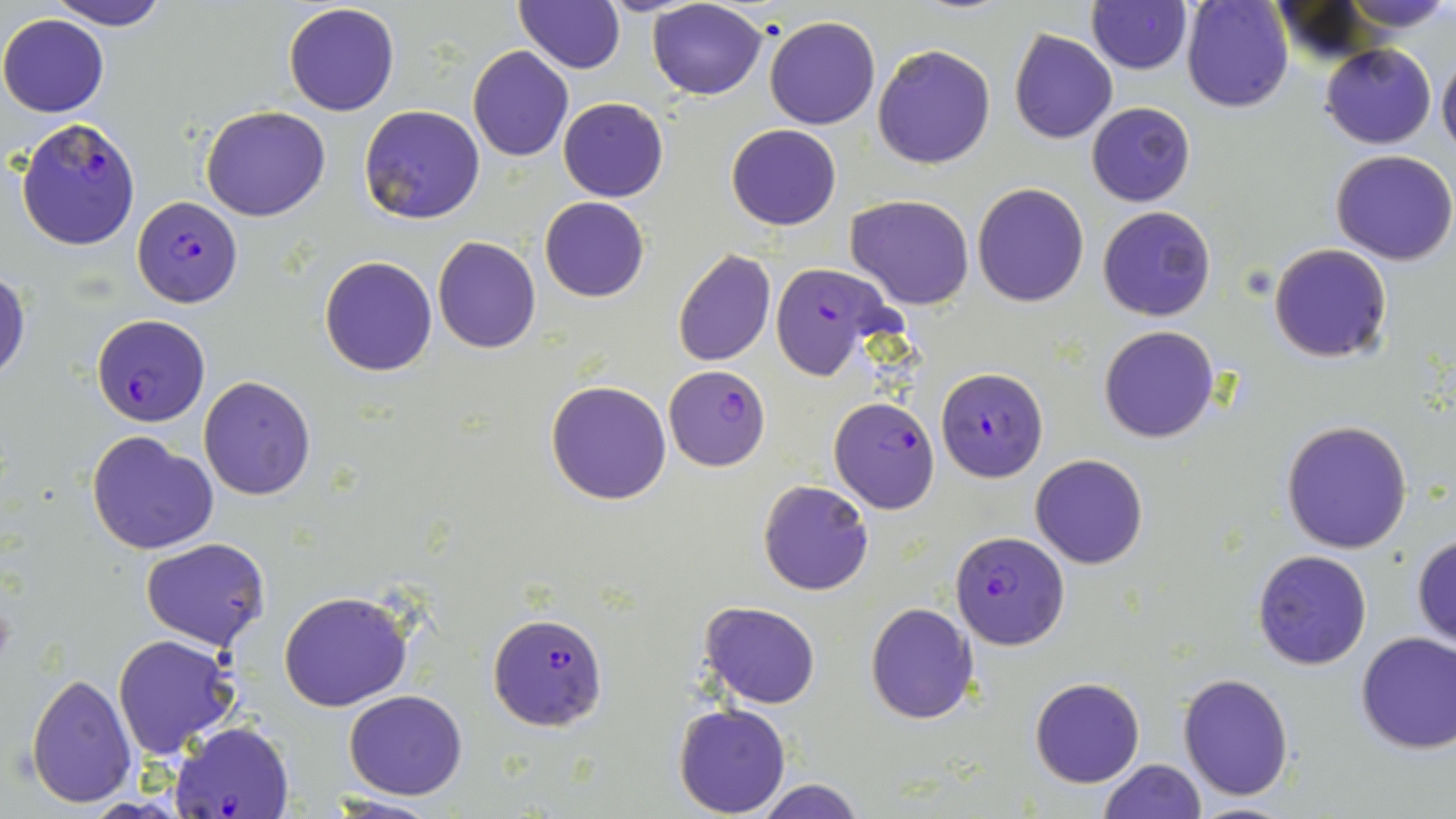

slide_level_diagnosis: Plasmodium falciparum
image_size: 1456×819 pixels
field_of_view: one of a larger specimen
modality: optical microscopy
uninfected_red_blood_cell_locations: 'approximate bounding boxes as named x1/y1/x2/y2 corners in pixels: (x1=48, y1=0, x2=170, y2=30), (x1=1182, y1=0, x2=1293, y2=113), (x1=1341, y1=0, x2=1452, y2=35), (x1=513, y1=1, x2=625, y2=73), (x1=1087, y1=1, x2=1192, y2=75), (x1=647, y1=2, x2=768, y2=99), (x1=282, y1=3, x2=400, y2=116), (x1=0, y1=12, x2=109, y2=117), (x1=763, y1=16, x2=881, y2=130), (x1=1009, y1=30, x2=1118, y2=145), (x1=872, y1=43, x2=996, y2=169), (x1=1320, y1=43, x2=1437, y2=148), (x1=467, y1=47, x2=575, y2=162), (x1=1437, y1=50, x2=1456, y2=159), (x1=558, y1=98, x2=669, y2=202), (x1=1086, y1=102, x2=1195, y2=206), (x1=359, y1=104, x2=486, y2=225), (x1=201, y1=105, x2=330, y2=221), (x1=726, y1=123, x2=842, y2=230), (x1=1331, y1=149, x2=1456, y2=264), (x1=972, y1=183, x2=1089, y2=306), (x1=846, y1=195, x2=976, y2=309), (x1=539, y1=197, x2=650, y2=302), (x1=1098, y1=205, x2=1216, y2=322), (x1=432, y1=236, x2=541, y2=354), (x1=1269, y1=243, x2=1392, y2=363), (x1=671, y1=250, x2=776, y2=366), (x1=319, y1=256, x2=438, y2=376), (x1=0, y1=269, x2=31, y2=387), (x1=1098, y1=325, x2=1221, y2=444), (x1=198, y1=375, x2=317, y2=501), (x1=546, y1=380, x2=672, y2=505), (x1=1281, y1=419, x2=1414, y2=555), (x1=87, y1=431, x2=220, y2=555), (x1=1030, y1=454, x2=1147, y2=569), (x1=758, y1=480, x2=874, y2=596), (x1=1411, y1=533, x2=1456, y2=650), (x1=140, y1=537, x2=270, y2=649), (x1=1252, y1=549, x2=1373, y2=670), (x1=279, y1=590, x2=413, y2=713), (x1=700, y1=602, x2=819, y2=710), (x1=865, y1=602, x2=979, y2=723), (x1=1354, y1=630, x2=1456, y2=753), (x1=113, y1=633, x2=239, y2=759), (x1=26, y1=673, x2=137, y2=808), (x1=1177, y1=673, x2=1295, y2=800), (x1=1030, y1=677, x2=1144, y2=787), (x1=343, y1=689, x2=469, y2=800), (x1=674, y1=701, x2=790, y2=817), (x1=1097, y1=759, x2=1205, y2=819), (x1=751, y1=778, x2=871, y2=818), (x1=322, y1=796, x2=445, y2=818), (x1=1183, y1=801, x2=1303, y2=819)'
plasmodium_falciparum_infected_red_blood_cell_locations: 'approximate bounding boxes as named x1/y1/x2/y2 corners in pixels: (x1=17, y1=116, x2=143, y2=252), (x1=133, y1=196, x2=243, y2=307), (x1=769, y1=262, x2=901, y2=383), (x1=91, y1=313, x2=211, y2=426), (x1=663, y1=365, x2=772, y2=471), (x1=936, y1=366, x2=1049, y2=480), (x1=829, y1=396, x2=940, y2=512), (x1=949, y1=530, x2=1070, y2=648), (x1=487, y1=612, x2=608, y2=731), (x1=169, y1=721, x2=293, y2=818)'
preparation: thin blood film
stain: May-Grünwald-Giemsa
magnification: 1000x